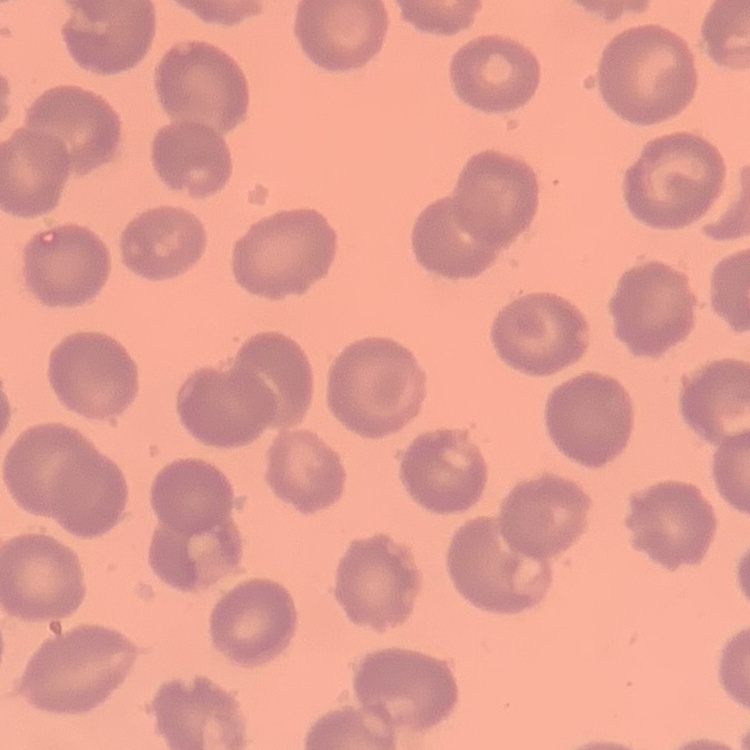
red blood cell morphology = no rouleaux formation
preparation = thin blood smear
image type = one tile cut from a larger photomicrograph
stain = Field's or Giemsa